Name the parasite shown.
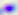

Toxoplasma gondii.

Photomicrograph. 400x magnification.